Identify the parasite.
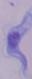
A trypanosome.

1000x magnification. Photomicrograph.